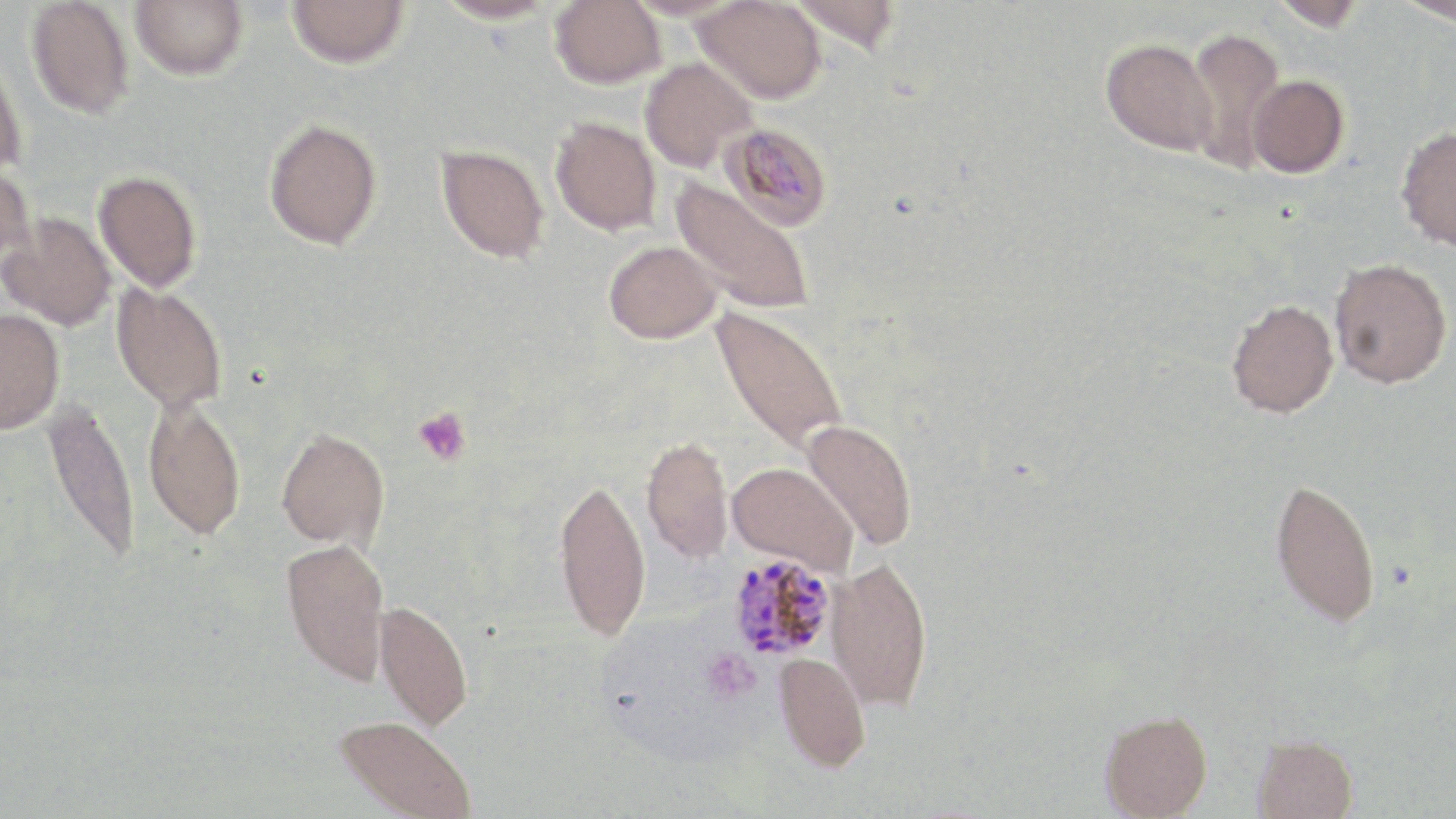

Approximate bounding boxes as (x1, y1, x2, y2) in pixels. Plasmodium malariae-infected red blood cell locations: (719, 121, 832, 231), (727, 552, 839, 660). Uninfected red blood cell locations: (26, 0, 135, 119), (129, 0, 248, 81), (286, 0, 410, 69), (432, 0, 560, 24), (550, 0, 666, 89), (622, 0, 742, 20), (789, 0, 901, 53), (1267, 0, 1370, 30), (1397, 0, 1456, 27), (693, 1, 825, 104), (1184, 27, 1287, 172), (1100, 38, 1218, 156), (0, 46, 28, 175), (639, 57, 757, 172), (1247, 74, 1349, 178), (550, 116, 661, 236), (263, 117, 383, 250), (1395, 126, 1456, 251), (436, 144, 549, 264), (0, 162, 37, 275), (93, 170, 202, 293), (669, 176, 815, 315), (1, 212, 117, 332), (604, 241, 723, 344), (1330, 259, 1451, 388), (110, 282, 228, 414), (1226, 299, 1338, 418), (710, 305, 850, 454), (0, 308, 64, 434), (142, 396, 247, 541), (39, 397, 140, 567), (800, 418, 917, 550), (275, 426, 389, 550), (641, 435, 733, 565), (727, 462, 859, 573), (553, 476, 651, 641), (1270, 477, 1381, 627), (280, 538, 390, 686), (826, 557, 933, 711), (374, 599, 474, 731), (773, 651, 871, 771), (1099, 710, 1212, 818), (335, 715, 476, 819), (1252, 733, 1358, 819). Platelet locations: (413, 407, 472, 466), (701, 648, 761, 704). Slide-level diagnosis: Plasmodium malariae. One field of a larger specimen. Image is 1456×819 pixels. Thin blood smear. May-Grünwald-Giemsa-stained preparation. Light microscopy. Captured at 1000x magnification.